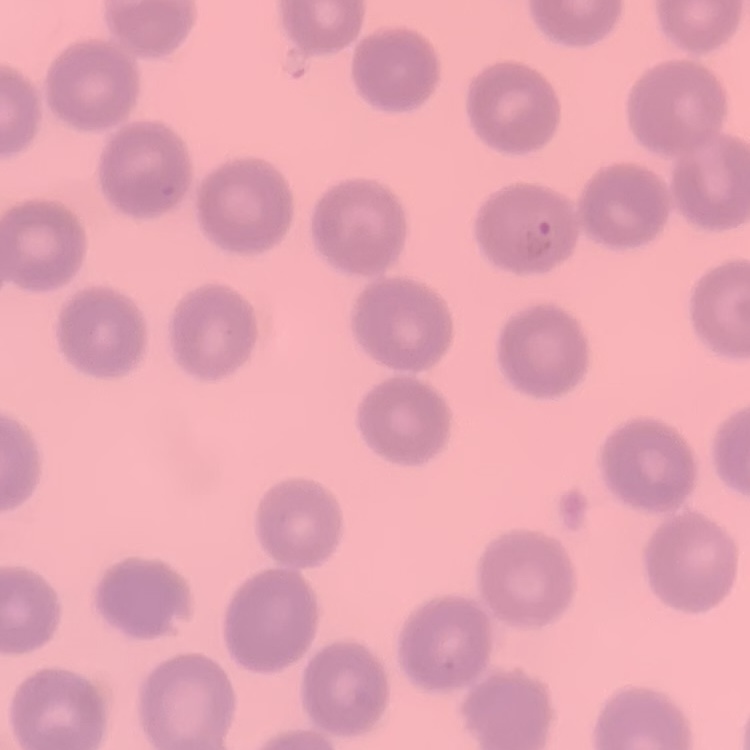

The red blood cells show no rouleaux formation. Thin peripheral smear. One tile cut from a larger photomicrograph. Field's or Giemsa stain.